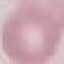

Malaria status: uninfected. Photographed with a smartphone camera at the microscope eyepiece. Thin blood smear. Cell patch, automatically extracted from a larger field of view and resized to 64 × 64 pixels. Giemsa stain.